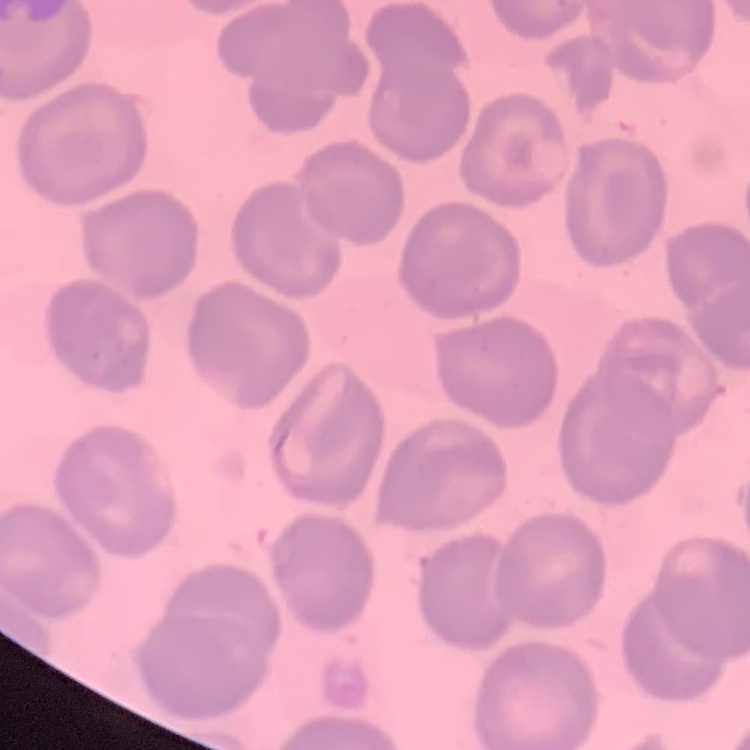
red blood cell morphology = no rouleaux formation
image type = one tile cut from a larger photomicrograph
preparation = thin blood smear
stain = Field's or Giemsa